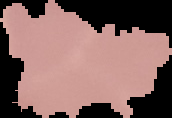

Summary:
  - Image type: segmented cell region with the area outside set to black
  - Image size: 172×118 pixels
  - Preparation: thin blood smear
  - Result: no Plasmodium parasites seen